Locate Plasmodium ovale parasites and identify their life-cycle stages.
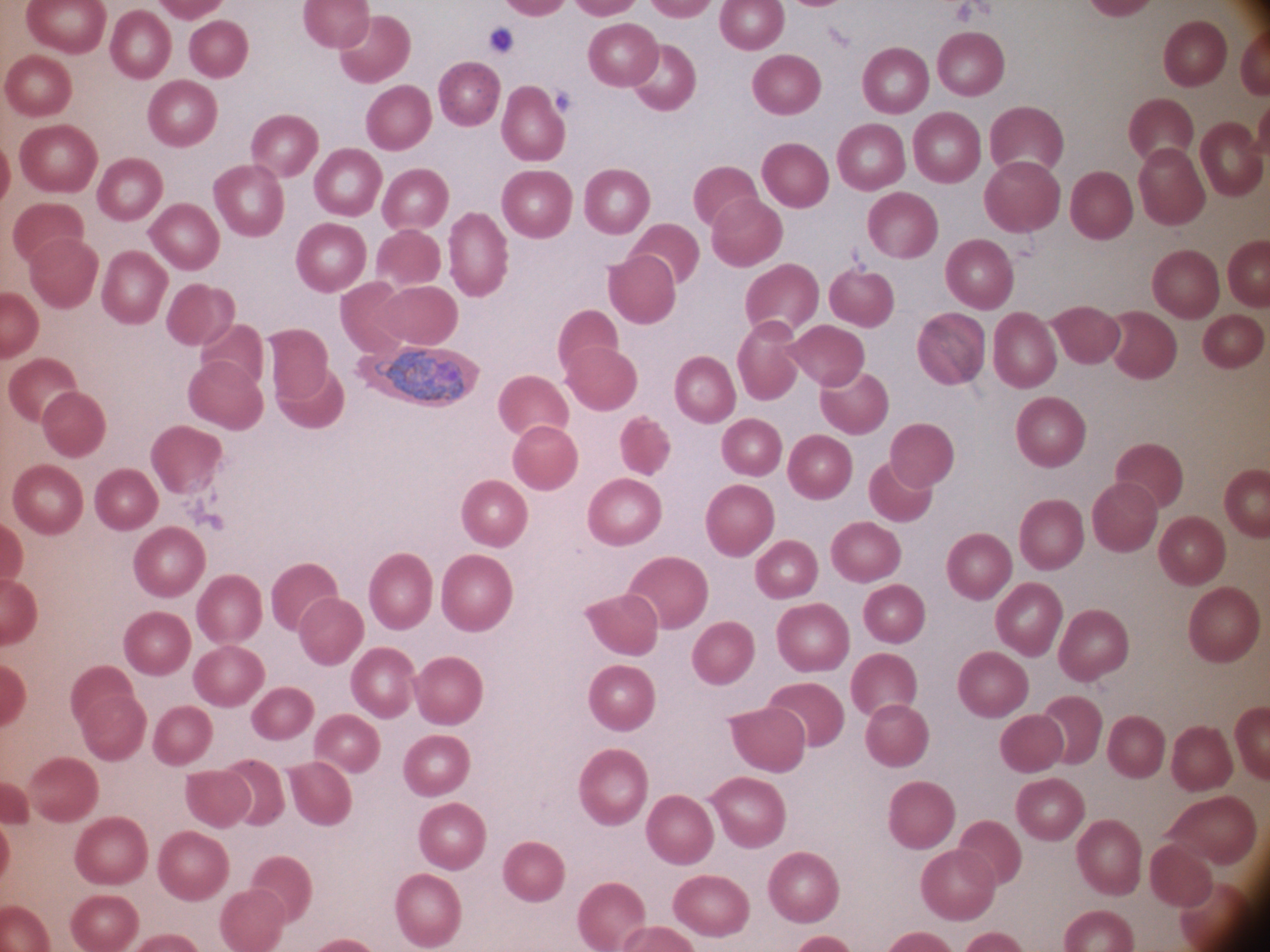

Approximate bounding boxes as (x1, y1, x2, y2) in pixels, from the source annotation, which is not necessarily exhaustive.
Trophozoites: (375, 350, 469, 407).

Summary:
  - Species: Plasmodium ovale
  - Microscope: Leica DM2000 with built-in camera
  - Magnification: 100x
  - Preparation: thin blood film
  - Image size: 1270×952 pixels
  - Stain: Giemsa
  - Field of view: single